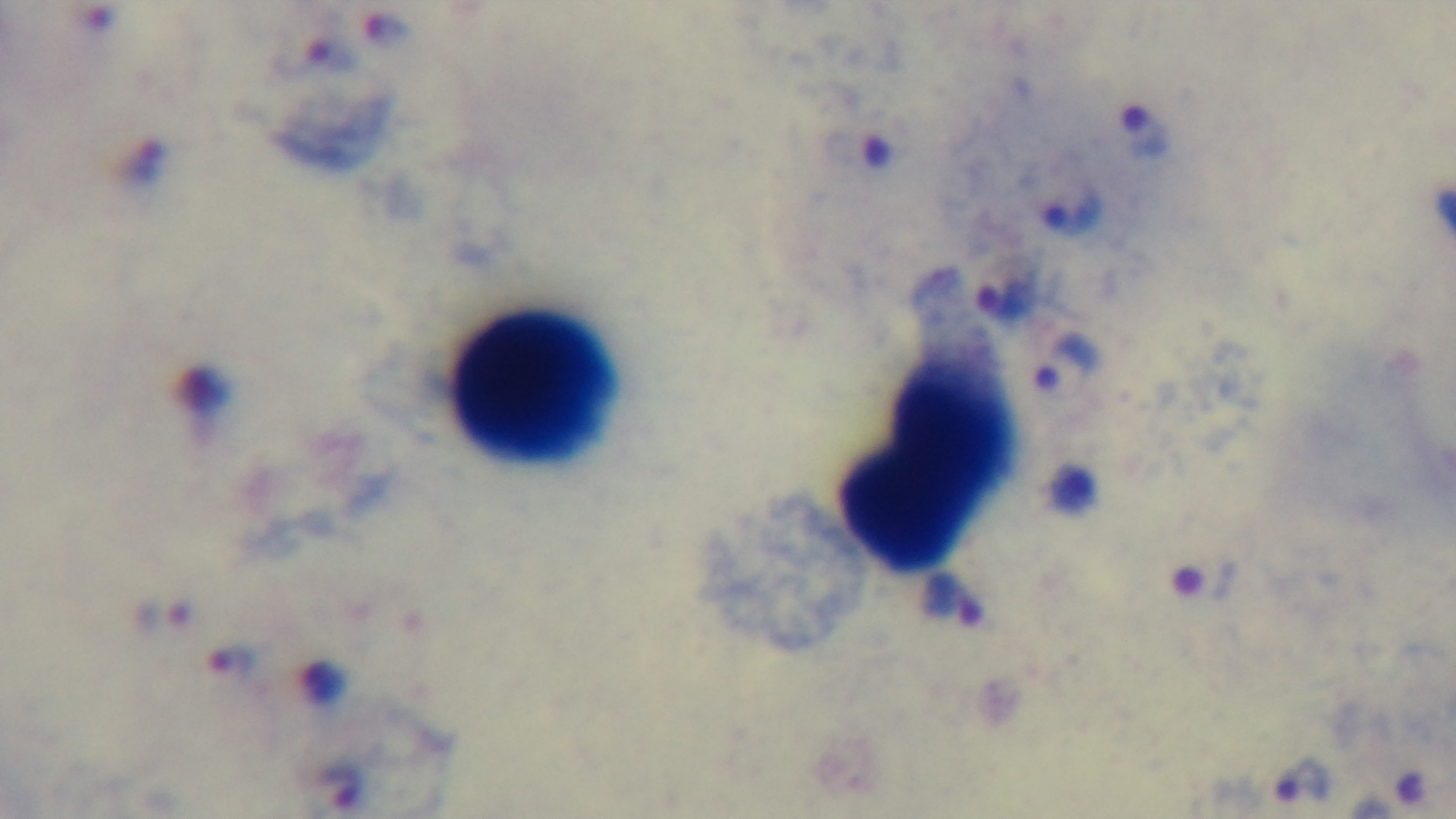

modality: light microscopy
objective: 100x oil immersion
preparation: thick smear
malaria_status: positive
field_of_view: one from the slide
capture: mounted 4K digital camera
stain: Giemsa